Point out each malaria parasite.
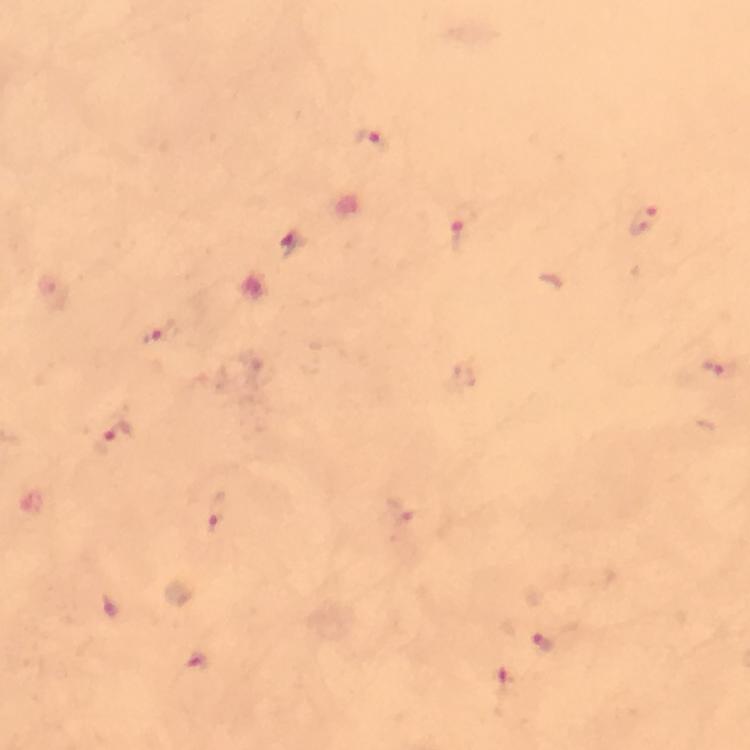

Approximate centers as [x, y] in pixels.
Malaria parasites: [372, 143], [642, 220], [458, 237], [291, 243], [159, 335], [722, 370], [116, 440], [218, 511], [401, 511], [544, 643].

immersion_oil: used
image_size: 750×750 pixels
capture: smartphone camera through the microscope
magnification: 100x
context: from a malaria diagnostic workup
stain: Giemsa
cropped_from: a single field of view
preparation: thick blood smear